Name the blood parasite species.
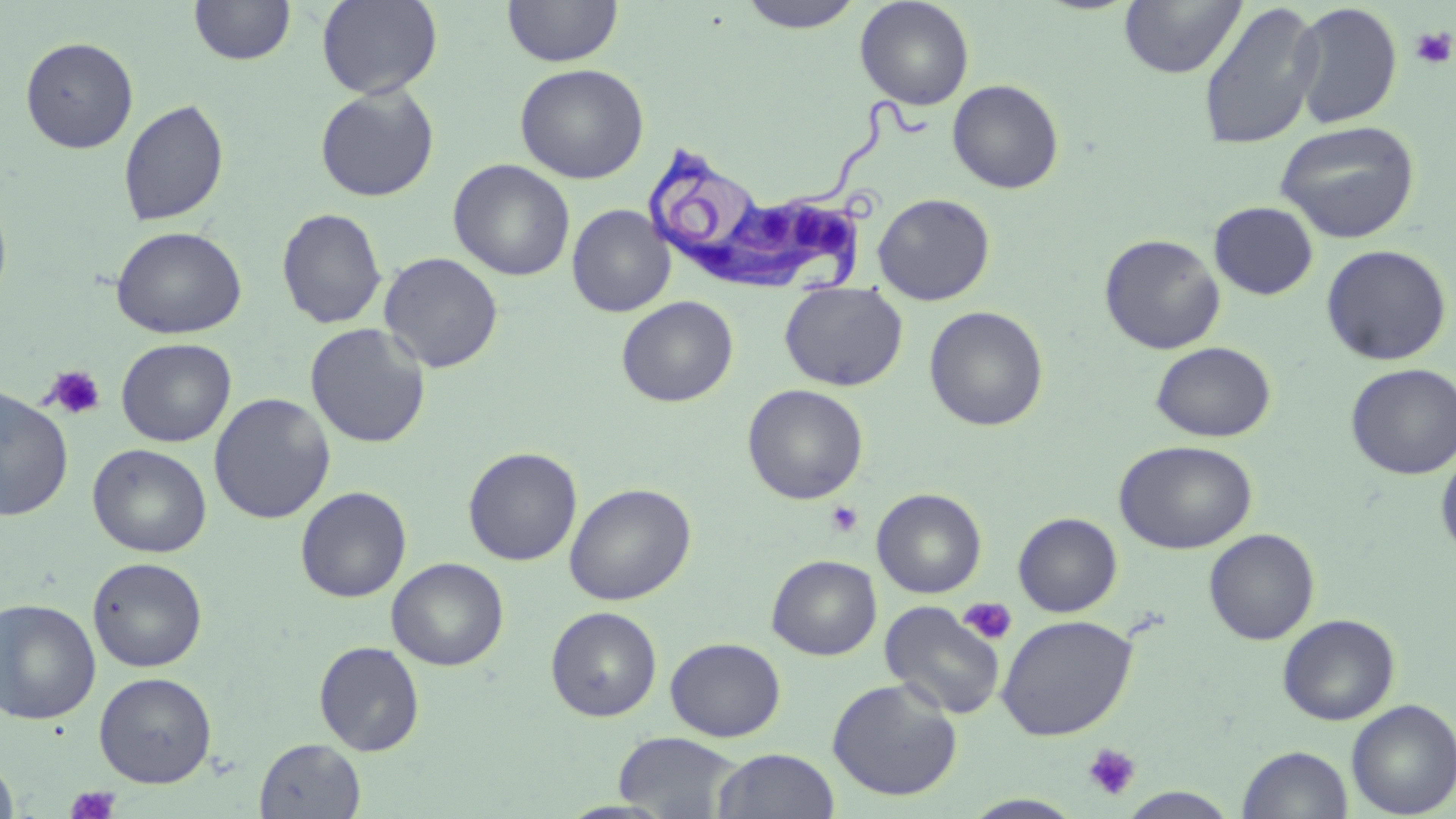
Trypanosoma brucei.

Approximate bounding boxes as named x1/y1/x2/y2 corners in pixels. Trypanosoma brucei locations: (x1=644, y1=97, x2=937, y2=296). Uninfected red blood cell locations: (x1=316, y1=0, x2=442, y2=100), (x1=502, y1=0, x2=623, y2=67), (x1=736, y1=0, x2=866, y2=33), (x1=855, y1=0, x2=975, y2=110), (x1=1119, y1=0, x2=1247, y2=79), (x1=189, y1=1, x2=295, y2=66), (x1=1290, y1=1, x2=1403, y2=130), (x1=1197, y1=2, x2=1323, y2=151), (x1=19, y1=36, x2=138, y2=154), (x1=514, y1=63, x2=649, y2=184), (x1=947, y1=79, x2=1064, y2=194), (x1=314, y1=85, x2=440, y2=202), (x1=118, y1=98, x2=230, y2=228), (x1=1274, y1=120, x2=1420, y2=243), (x1=449, y1=159, x2=575, y2=281), (x1=0, y1=191, x2=13, y2=310), (x1=872, y1=192, x2=996, y2=305), (x1=1209, y1=201, x2=1318, y2=300), (x1=566, y1=204, x2=675, y2=317), (x1=276, y1=207, x2=388, y2=329), (x1=111, y1=226, x2=247, y2=339), (x1=1099, y1=233, x2=1225, y2=354), (x1=1321, y1=244, x2=1452, y2=366), (x1=379, y1=252, x2=503, y2=373), (x1=779, y1=284, x2=907, y2=391), (x1=616, y1=296, x2=738, y2=407), (x1=924, y1=305, x2=1049, y2=432), (x1=304, y1=323, x2=431, y2=448), (x1=106, y1=338, x2=224, y2=559), (x1=116, y1=338, x2=236, y2=447), (x1=1151, y1=341, x2=1276, y2=442), (x1=1345, y1=363, x2=1456, y2=480), (x1=742, y1=383, x2=868, y2=505), (x1=0, y1=385, x2=74, y2=521), (x1=209, y1=392, x2=335, y2=524), (x1=1114, y1=439, x2=1257, y2=554), (x1=88, y1=443, x2=212, y2=557), (x1=463, y1=446, x2=582, y2=566), (x1=1435, y1=450, x2=1456, y2=560), (x1=564, y1=482, x2=696, y2=606), (x1=295, y1=486, x2=411, y2=602), (x1=871, y1=488, x2=987, y2=598), (x1=1013, y1=512, x2=1123, y2=617), (x1=1203, y1=528, x2=1320, y2=645), (x1=767, y1=555, x2=882, y2=660), (x1=87, y1=556, x2=208, y2=673), (x1=386, y1=557, x2=509, y2=670), (x1=0, y1=597, x2=101, y2=725), (x1=880, y1=601, x2=1006, y2=720), (x1=545, y1=606, x2=662, y2=721), (x1=1278, y1=613, x2=1400, y2=725), (x1=997, y1=614, x2=1137, y2=741), (x1=665, y1=637, x2=786, y2=742), (x1=313, y1=641, x2=425, y2=756), (x1=94, y1=672, x2=217, y2=787), (x1=826, y1=677, x2=963, y2=802), (x1=1346, y1=699, x2=1456, y2=818), (x1=613, y1=731, x2=746, y2=817), (x1=255, y1=737, x2=365, y2=818), (x1=1236, y1=745, x2=1353, y2=819), (x1=712, y1=748, x2=840, y2=819), (x1=0, y1=752, x2=18, y2=818), (x1=1119, y1=787, x2=1239, y2=818), (x1=961, y1=793, x2=1087, y2=818). Platelet locations: (x1=1410, y1=27, x2=1455, y2=69), (x1=44, y1=364, x2=107, y2=421), (x1=824, y1=500, x2=865, y2=539), (x1=957, y1=597, x2=1018, y2=645), (x1=1082, y1=743, x2=1142, y2=800), (x1=65, y1=785, x2=121, y2=819). Thin blood smear. Captured at 1000x magnification. May-Grünwald-Giemsa-stained preparation. Image is 1456×819 pixels. One field of a larger specimen. Optical microscopy.